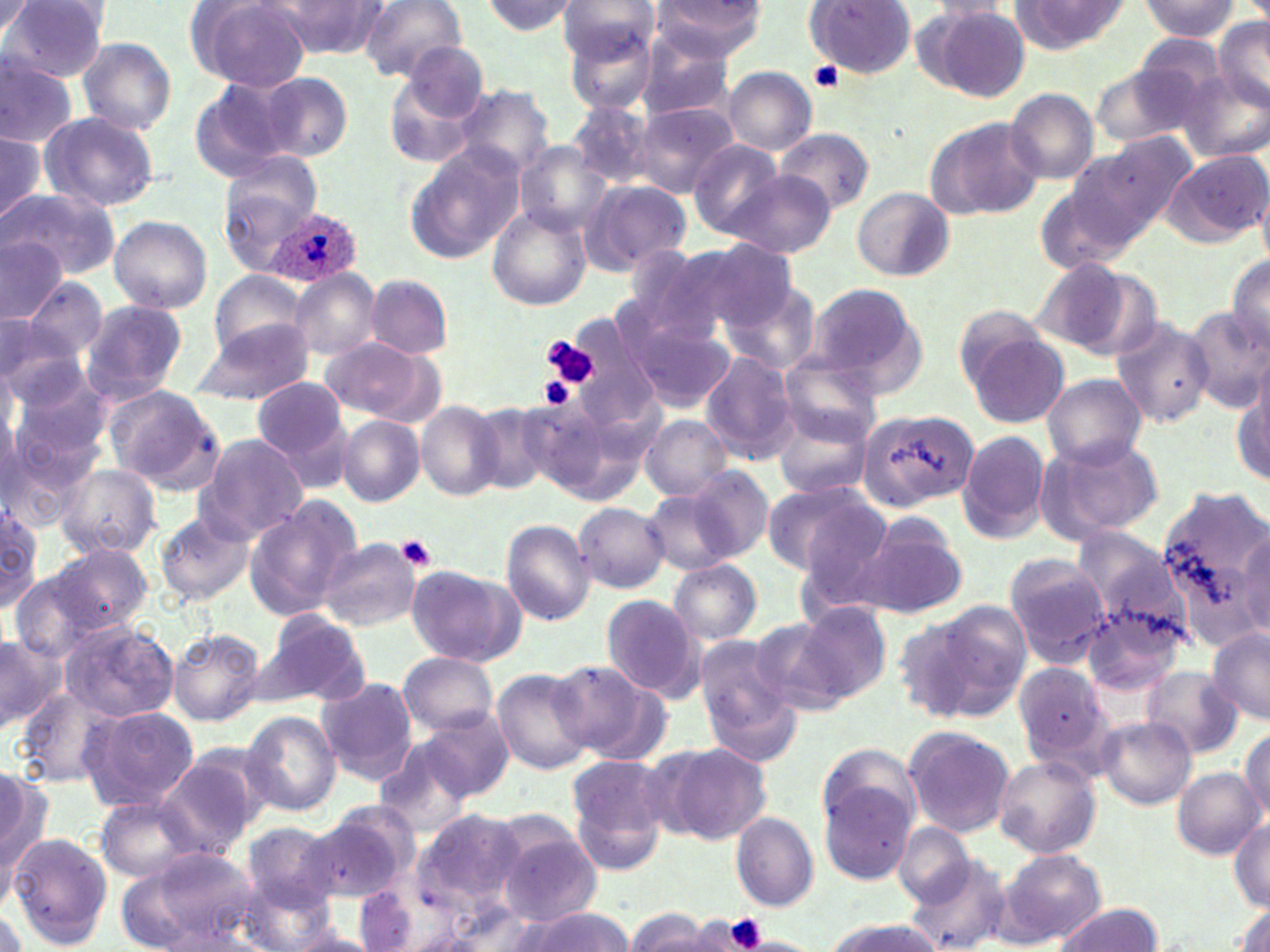

Summary:
  - Coordinate format: approximate bounding boxes as (x1, y1, x2, y2) in pixels
  - Platelet locations: (809, 62, 846, 92), (542, 335, 598, 386), (541, 377, 579, 409), (395, 534, 438, 570), (721, 913, 770, 952)
  - Plasmodium ovale-infected red blood cell locations: (266, 208, 361, 289)
  - Uninfected red blood cell locations: (190, 0, 313, 93), (357, 0, 468, 81), (558, 0, 660, 67), (3, 1, 109, 81), (477, 1, 579, 37), (649, 1, 768, 63), (805, 1, 918, 81), (923, 1, 1013, 20), (1010, 1, 1132, 53), (1138, 1, 1241, 40), (0, 2, 34, 40), (273, 2, 391, 57), (921, 6, 1031, 101), (1214, 17, 1269, 114), (562, 18, 661, 113), (1129, 30, 1237, 126), (633, 32, 737, 121), (77, 37, 176, 136), (398, 41, 490, 127), (0, 57, 79, 147), (1092, 59, 1211, 150), (723, 66, 817, 155), (385, 72, 484, 170), (1179, 72, 1268, 162), (256, 73, 352, 160), (188, 80, 296, 183), (450, 85, 555, 180), (1005, 88, 1100, 184), (567, 98, 658, 188), (631, 102, 737, 198), (39, 112, 160, 213), (924, 115, 1045, 220), (0, 128, 47, 228), (775, 129, 876, 215), (1076, 133, 1197, 246), (688, 139, 787, 237), (516, 144, 610, 235), (405, 148, 524, 262), (1161, 150, 1270, 247), (220, 152, 321, 268), (726, 170, 834, 258), (581, 180, 690, 272), (851, 186, 955, 281), (6, 189, 120, 278), (487, 206, 591, 311), (108, 216, 212, 313), (0, 236, 66, 322), (680, 242, 801, 338), (1225, 255, 1270, 354), (1031, 260, 1151, 356), (209, 270, 309, 359), (291, 270, 380, 359), (365, 275, 453, 358), (24, 280, 107, 363), (721, 280, 821, 374), (803, 282, 925, 394), (78, 299, 188, 403), (1183, 308, 1269, 411), (628, 310, 736, 414), (0, 313, 51, 383), (0, 315, 83, 409), (1111, 316, 1215, 427), (191, 317, 315, 406), (961, 326, 1067, 428), (319, 339, 438, 420), (700, 350, 799, 461), (779, 353, 884, 444), (5, 372, 112, 479), (1043, 374, 1145, 470), (252, 377, 349, 464), (1233, 383, 1267, 485), (103, 385, 224, 491), (417, 402, 505, 500), (474, 404, 562, 497), (771, 406, 874, 501), (858, 406, 978, 512), (266, 408, 358, 494), (641, 415, 732, 500), (337, 416, 424, 506), (957, 429, 1051, 543), (0, 433, 88, 535), (195, 433, 311, 542), (1040, 434, 1165, 539), (57, 465, 160, 557), (678, 465, 775, 565), (758, 480, 883, 577), (1155, 482, 1270, 648), (642, 487, 746, 576), (244, 498, 360, 620), (573, 502, 670, 593), (0, 504, 44, 608), (855, 511, 968, 620), (155, 512, 255, 605), (499, 517, 596, 625), (318, 536, 421, 631), (54, 543, 152, 635), (1004, 554, 1112, 666), (669, 561, 762, 644), (407, 565, 524, 667), (8, 570, 107, 663), (601, 595, 705, 702), (1079, 595, 1187, 701), (924, 599, 1033, 717), (795, 602, 891, 702), (259, 610, 370, 707), (893, 611, 993, 725), (750, 616, 862, 718), (59, 620, 179, 723), (1205, 628, 1270, 723), (168, 629, 264, 725), (0, 631, 65, 732), (698, 649, 804, 766), (396, 651, 499, 737), (551, 661, 656, 757), (1014, 661, 1118, 774), (1141, 666, 1241, 759), (492, 669, 595, 776), (315, 678, 417, 781), (16, 687, 121, 786), (79, 706, 198, 811), (409, 708, 513, 804), (242, 709, 341, 816), (1097, 717, 1196, 810), (1239, 724, 1270, 822), (902, 725, 1016, 838), (373, 736, 490, 837), (817, 741, 920, 845), (660, 744, 772, 846), (155, 751, 264, 859), (994, 755, 1101, 857), (566, 756, 674, 871), (0, 765, 51, 891), (1172, 768, 1263, 858), (819, 780, 916, 883), (96, 798, 199, 882), (310, 802, 417, 902), (405, 806, 532, 931), (730, 812, 818, 911), (1230, 817, 1270, 910), (492, 819, 603, 924), (243, 821, 342, 911), (893, 823, 975, 906), (7, 833, 111, 949), (133, 847, 261, 947), (1000, 850, 1105, 946), (903, 861, 1010, 950), (111, 866, 209, 950), (240, 876, 337, 952), (353, 885, 421, 952), (1229, 903, 1270, 952), (1053, 904, 1160, 952), (507, 908, 636, 952), (626, 910, 709, 950), (689, 914, 767, 951), (276, 919, 382, 952), (820, 919, 945, 951)
  - Slide-level diagnosis: Plasmodium ovale
  - Magnification: 1000x
  - Stain: May-Grünwald-Giemsa
  - Image size: 1270×952 pixels
  - Preparation: thin blood smear
  - Modality: light microscopy
  - Field of view: single